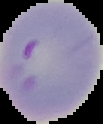
Summary:
  - Preparation: thin blood smear
  - Malaria status: parasitized
  - Image size: 103×124 pixels
  - Image type: segmented cell region on a black background